Report the malaria status of this cell.
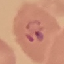
It is parasitized.

Summary:
  - Image type: automatically extracted cell patch, resized to 64 × 64 pixels
  - Preparation: thin smear
  - Capture: smartphone camera at the microscope eyepiece
  - Stain: Giemsa